Assess the morphology of the red blood cells.
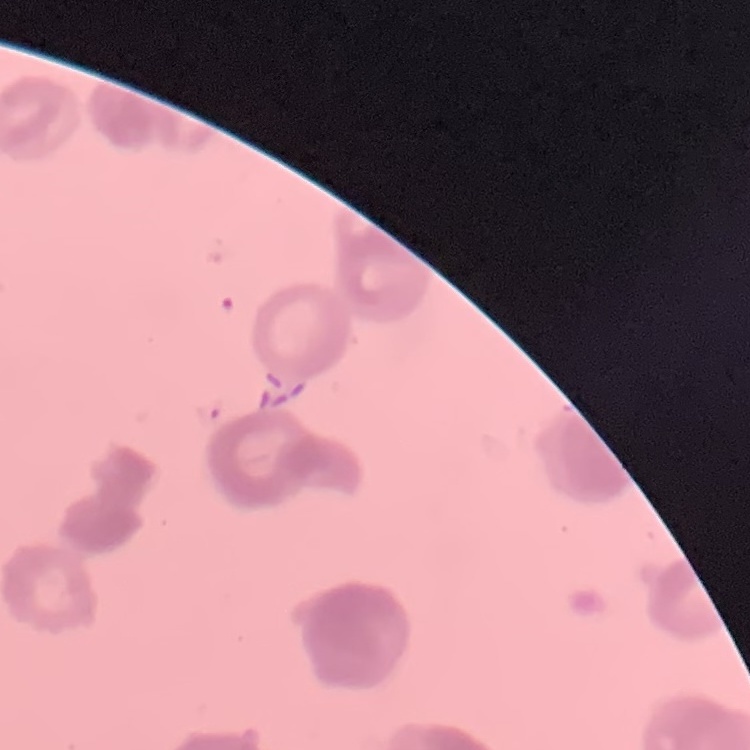
They show rouleaux formation.

Square crop of a larger photomicrograph. Thin blood smear. Field's or Giemsa stain.